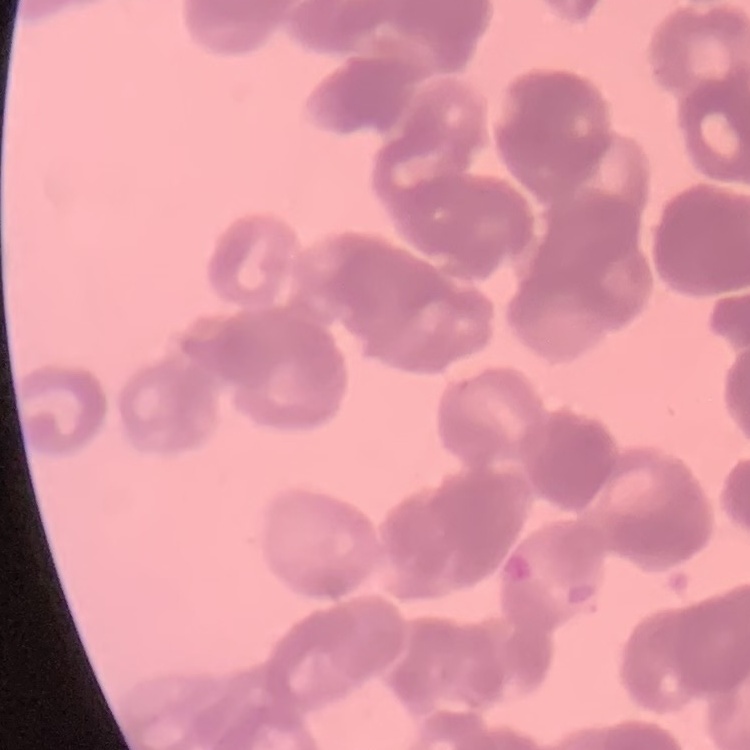
The erythrocytes show rouleaux formation. Stained with either Field's or Giemsa. One tile cut from a larger photomicrograph. Thin peripheral smear.